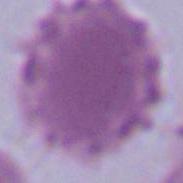

magnification = 1000x
identification = erythrocyte
modality = photomicrograph